Locate every leukocyte (white blood cell).
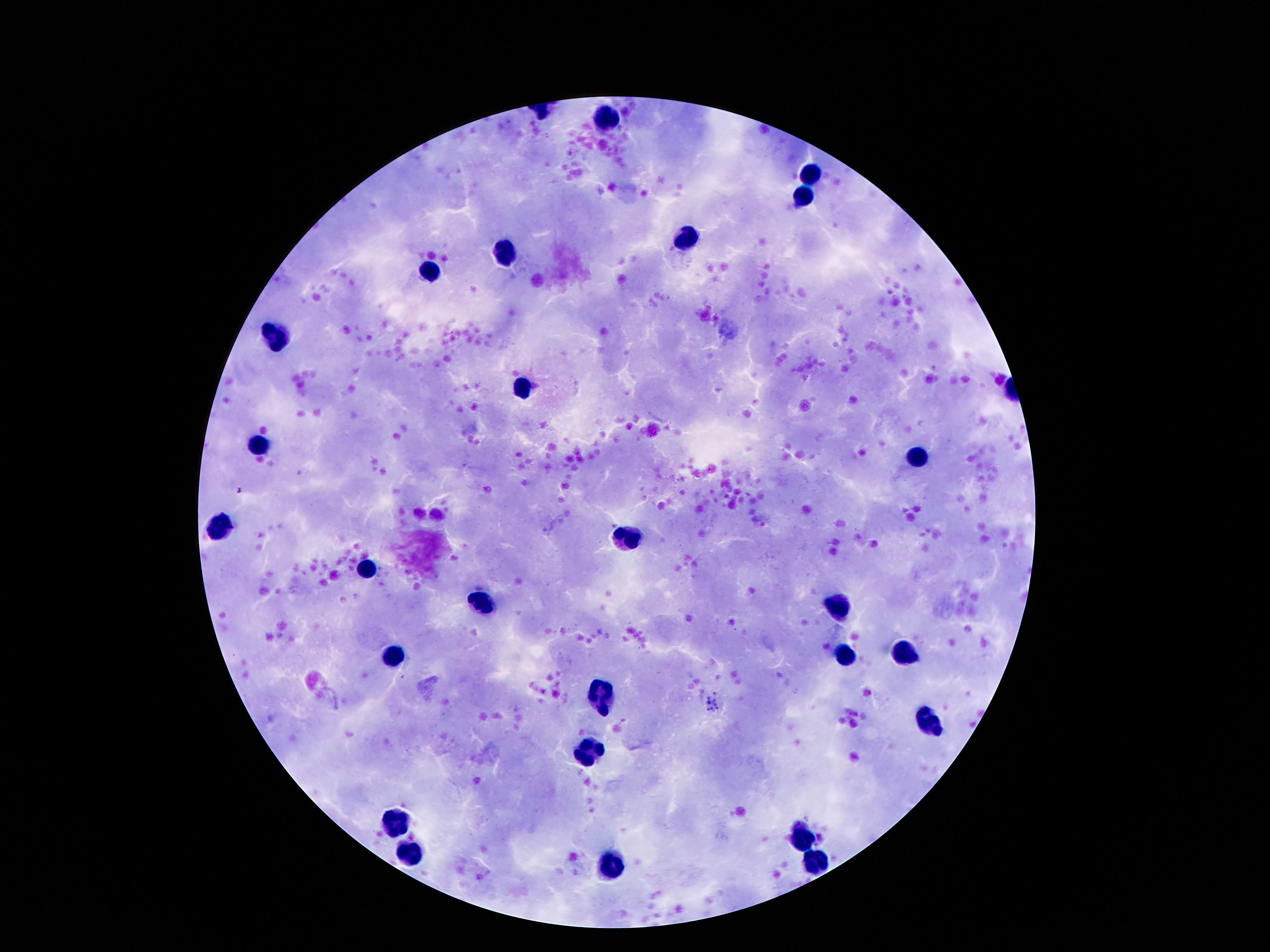

Approximate object centers, in pixels from the top-left corner.
Leukocytes: (x=609, y=121), (x=812, y=174), (x=802, y=197), (x=685, y=242), (x=505, y=252), (x=431, y=271), (x=277, y=334), (x=523, y=387), (x=259, y=444), (x=912, y=457), (x=220, y=526), (x=626, y=535), (x=367, y=569), (x=843, y=602), (x=480, y=603), (x=906, y=651), (x=396, y=654), (x=845, y=657), (x=601, y=696), (x=931, y=721), (x=589, y=748), (x=396, y=819), (x=804, y=838), (x=415, y=850), (x=820, y=860), (x=613, y=866).

Thick peripheral-blood smear. Giemsa-stained preparation. 100x magnification. Photographed through the microscope eyepiece with a smartphone camera. Image is 1270×952 pixels. Single field of view. Patient malaria status: negative.